Report the malaria status of this cell.
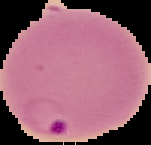
It is parasitized.

{
  "preparation": "thin blood smear",
  "image_size": "151×145 pixels",
  "image_type": "segmented cell region on a black background"
}